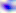
Captured at 400x magnification. Photomicrograph. Toxoplasma gondii is shown.